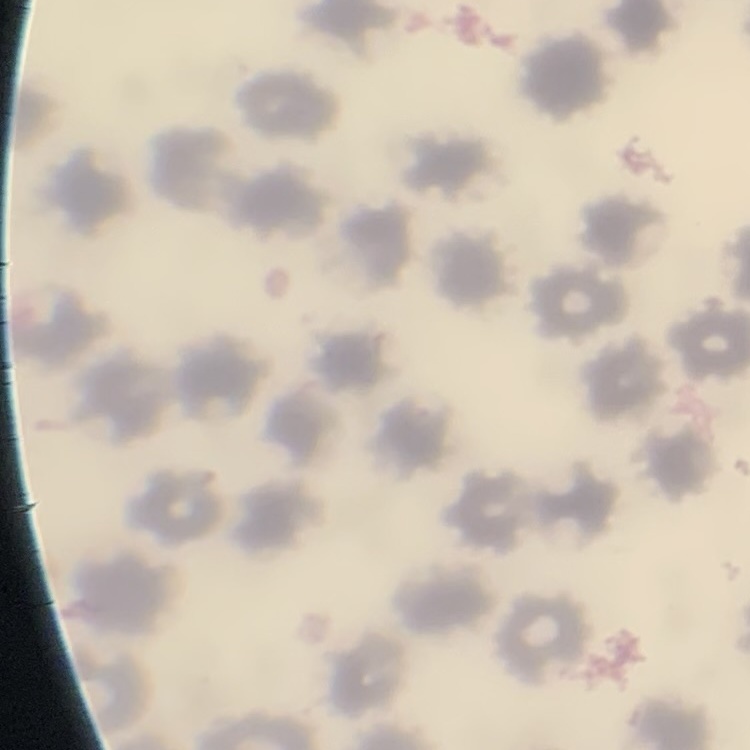

Summary:
  - Erythrocyte morphology: no rouleaux formation
  - Preparation: thin blood smear
  - Image type: one tile cut from a larger photomicrograph
  - Stain: Field's or Giemsa